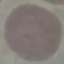

Summary:
  - Malaria status: uninfected
  - Image type: automatically extracted cell patch, resized to 64 × 64 pixels
  - Capture: smartphone through the microscope eyepiece
  - Stain: Giemsa
  - Preparation: thin smear